Assess this cell for malaria.
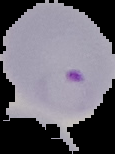

It is parasitized.

Summary:
  - Image type: segmented cell region with the area outside set to black
  - Preparation: thin blood film
  - Image size: 115×154 pixels